Comment on the morphology of the red blood cells.
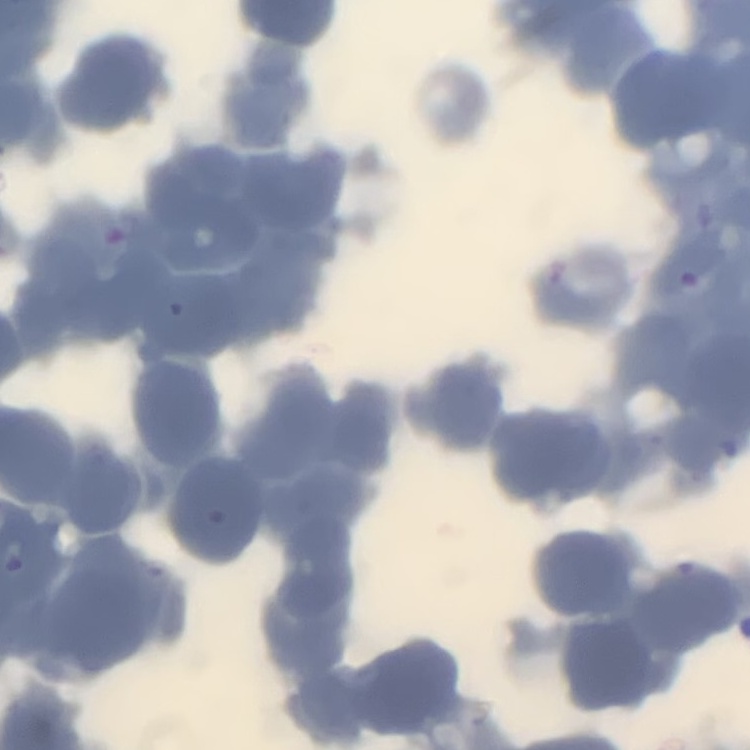
Rouleaux formation.

Square crop of a larger photomicrograph. Thin blood film. Field's or Giemsa stain.